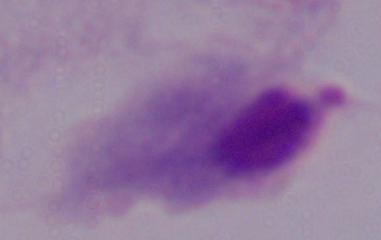
Photomicrograph. 1000x magnification. A trichomonad is shown.